Comment on the morphology of the erythrocytes.
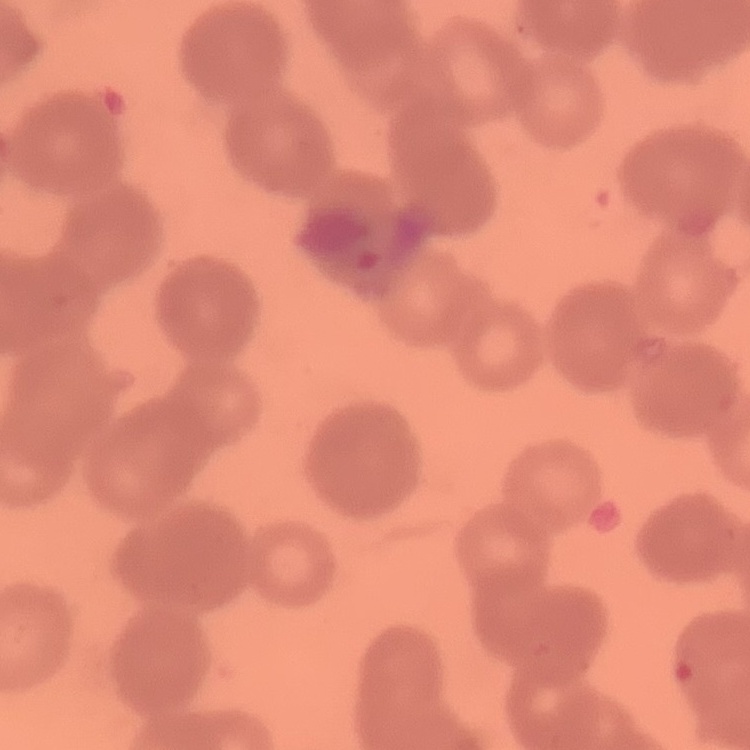
They show rouleaux formation.

preparation = thin blood film
stain = Field's or Giemsa
image type = one tile cut from a larger photomicrograph